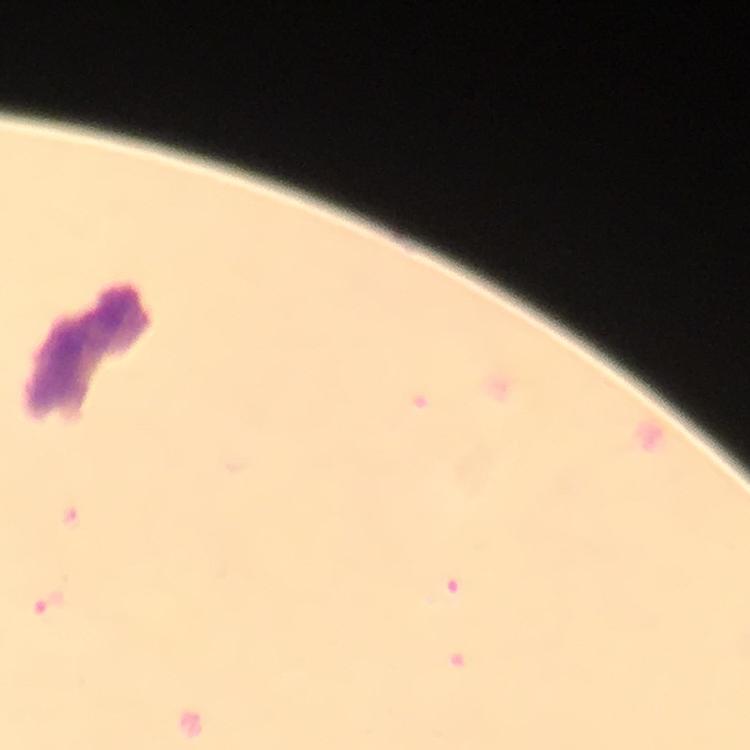 Approximate centers as [x, y] in pixels. Malaria parasite locations: [460, 596], [51, 602]. Smartphone photograph taken through a microscope. Immersion oil applied. Image is 750×750 pixels. From a malaria diagnostic workup. A crop from one field of view. Giemsa stain. At 100x magnification. Thick blood film.